Locate every blood parasite and identify its species.
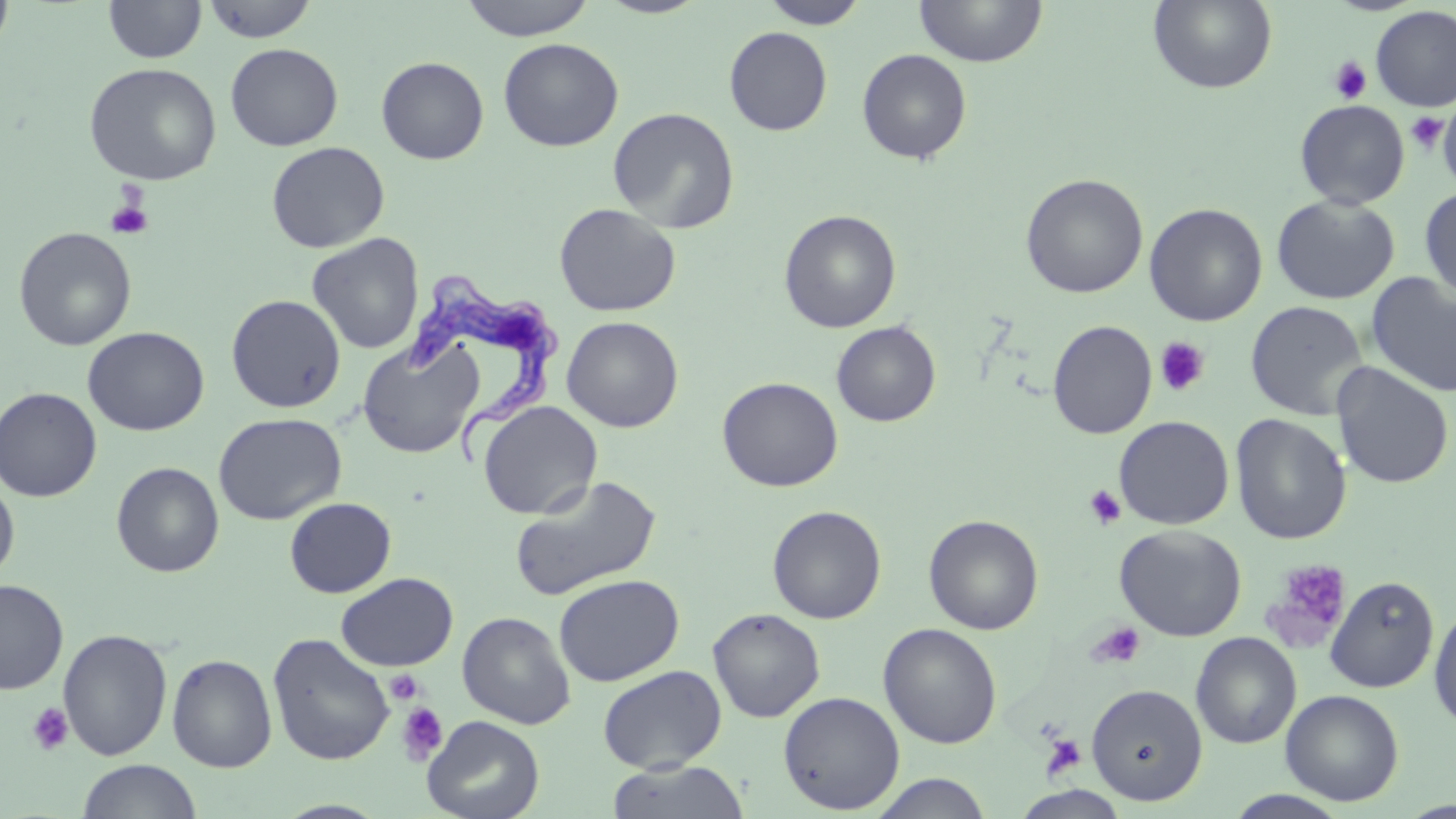

Approximate bounding boxes as [x1, y1, x2, y2] in pixels.
Trypanosoma brucei: [402, 273, 560, 466].
No Plasmodium falciparum, Plasmodium ovale, Plasmodium malariae, Plasmodium vivax, or Babesia divergens observed.

{
  "slide_level_diagnosis": "Trypanosoma brucei",
  "platelet_locations": "approximate bounding boxes as [x1, y1, x2, y2] in pixels: [1328, 57, 1372, 104], [1406, 111, 1449, 155], [104, 196, 153, 239], [1154, 337, 1211, 397], [1084, 484, 1127, 530], [1264, 559, 1352, 649], [1087, 621, 1146, 670], [386, 670, 424, 704], [27, 703, 73, 756], [397, 703, 448, 765], [1039, 734, 1087, 781]",
  "stain": "May-Grünwald-Giemsa",
  "uninfected_red_blood_cell_locations": "approximate bounding boxes as [x1, y1, x2, y2] in pixels: [1, 0, 16, 60], [103, 0, 206, 63], [458, 0, 597, 41], [595, 0, 711, 19], [759, 0, 869, 29], [913, 0, 1047, 67], [1148, 0, 1278, 94], [201, 1, 318, 43], [1370, 5, 1456, 112], [724, 26, 833, 135], [498, 38, 624, 152], [225, 43, 344, 151], [856, 49, 972, 164], [376, 56, 489, 164], [83, 62, 222, 186], [1294, 99, 1410, 210], [1438, 102, 1455, 192], [607, 107, 740, 233], [266, 141, 389, 253], [1020, 173, 1148, 299], [1419, 187, 1456, 302], [1271, 194, 1400, 305], [554, 203, 681, 317], [1144, 203, 1268, 326], [779, 209, 901, 333], [13, 227, 137, 351], [307, 233, 424, 355], [1365, 271, 1456, 398], [226, 294, 346, 413], [1245, 300, 1369, 421], [561, 316, 683, 432], [1047, 319, 1157, 439], [831, 321, 941, 427], [82, 326, 209, 436], [357, 337, 484, 458], [1331, 362, 1454, 489], [717, 376, 843, 492], [0, 387, 102, 502], [477, 401, 602, 520], [213, 412, 346, 525], [1229, 414, 1351, 545], [1113, 416, 1235, 529], [111, 461, 224, 577], [510, 474, 662, 601], [0, 477, 19, 583], [284, 497, 396, 598], [767, 505, 886, 624], [924, 514, 1044, 635], [1114, 524, 1247, 641], [336, 572, 458, 671], [554, 574, 684, 686], [1324, 575, 1439, 693], [0, 579, 68, 695], [1428, 602, 1456, 732], [708, 608, 825, 723], [457, 611, 576, 729], [878, 623, 1002, 748], [58, 628, 173, 761], [1190, 632, 1302, 749], [267, 633, 395, 766], [167, 653, 278, 772], [597, 664, 727, 773], [1087, 683, 1208, 805], [1281, 689, 1404, 806], [778, 691, 905, 814], [422, 715, 544, 819], [77, 759, 201, 818], [605, 760, 752, 818], [868, 773, 995, 818], [1224, 790, 1353, 819], [273, 799, 392, 818]",
  "modality": "optical microscopy",
  "field_of_view": "one of a larger specimen",
  "magnification": "1000x",
  "image_size": "1456×819 pixels",
  "preparation": "thin blood smear"
}